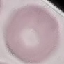 Malaria status: uninfected. Thin blood smear. Giemsa stain. Photographed with a smartphone camera at the microscope eyepiece. Cell patch, automatically extracted from a larger field of view and resized to 64 × 64 pixels.